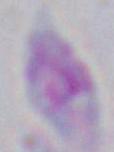
Summary:
  - Magnification: 1000x
  - Identification: Toxoplasma gondii
  - Modality: photomicrograph